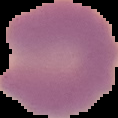
{
  "preparation": "thin blood film",
  "malaria_status": "parasitized",
  "image_size": "118×118 pixels",
  "image_type": "segmented cell region on a black background"
}